Classify this cell by malaria status.
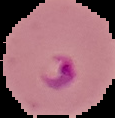
It is parasitized.

Cell region segmented out of the field of view; the surrounding area is masked to black. From a thin blood film. Image is 115×118 pixels.